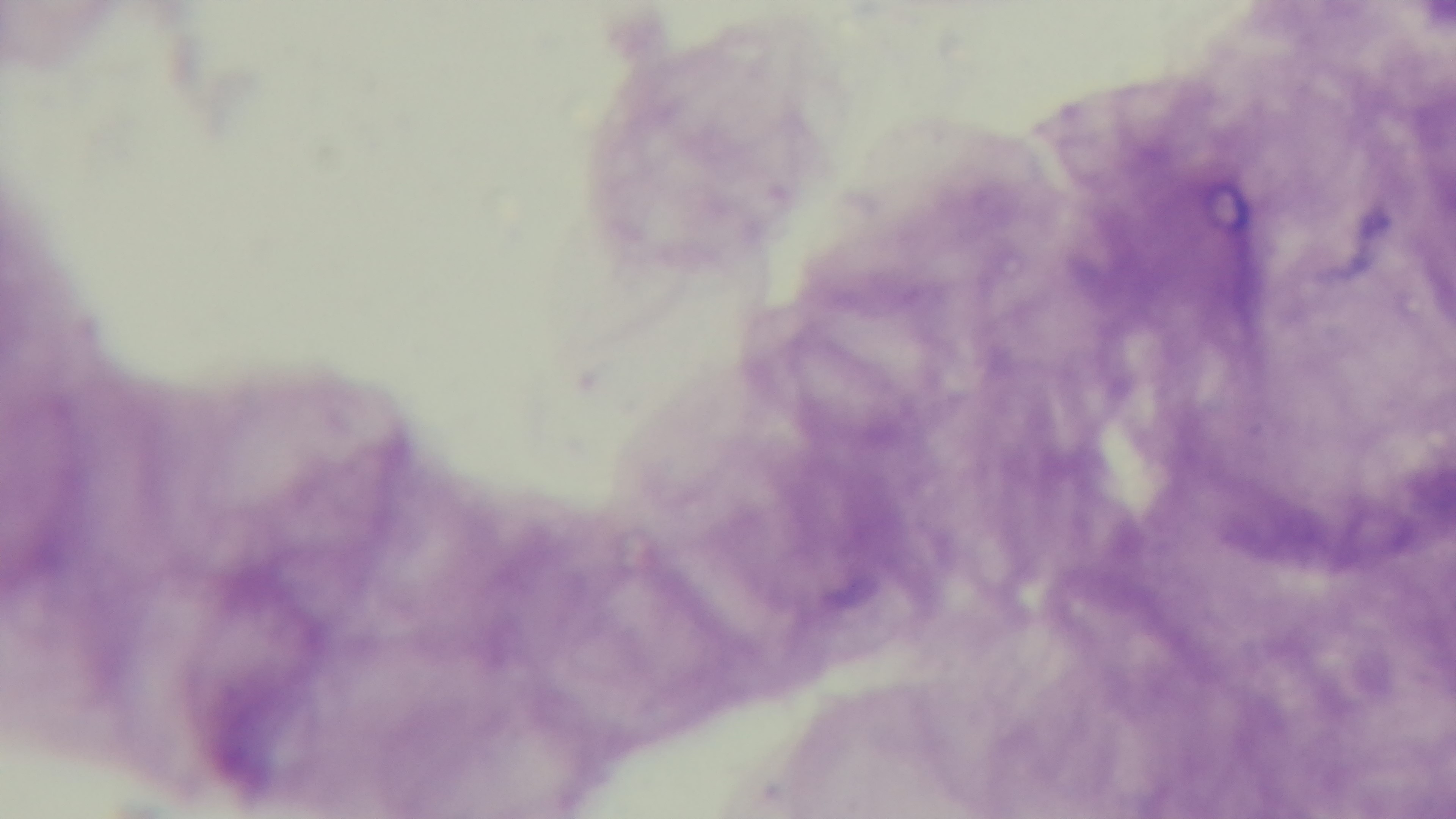
objective: 100x oil immersion
malaria_status: uninfected
capture: mounted 4K digital camera
modality: light microscopy
field_of_view: single
preparation: thick smear
stain: Giemsa